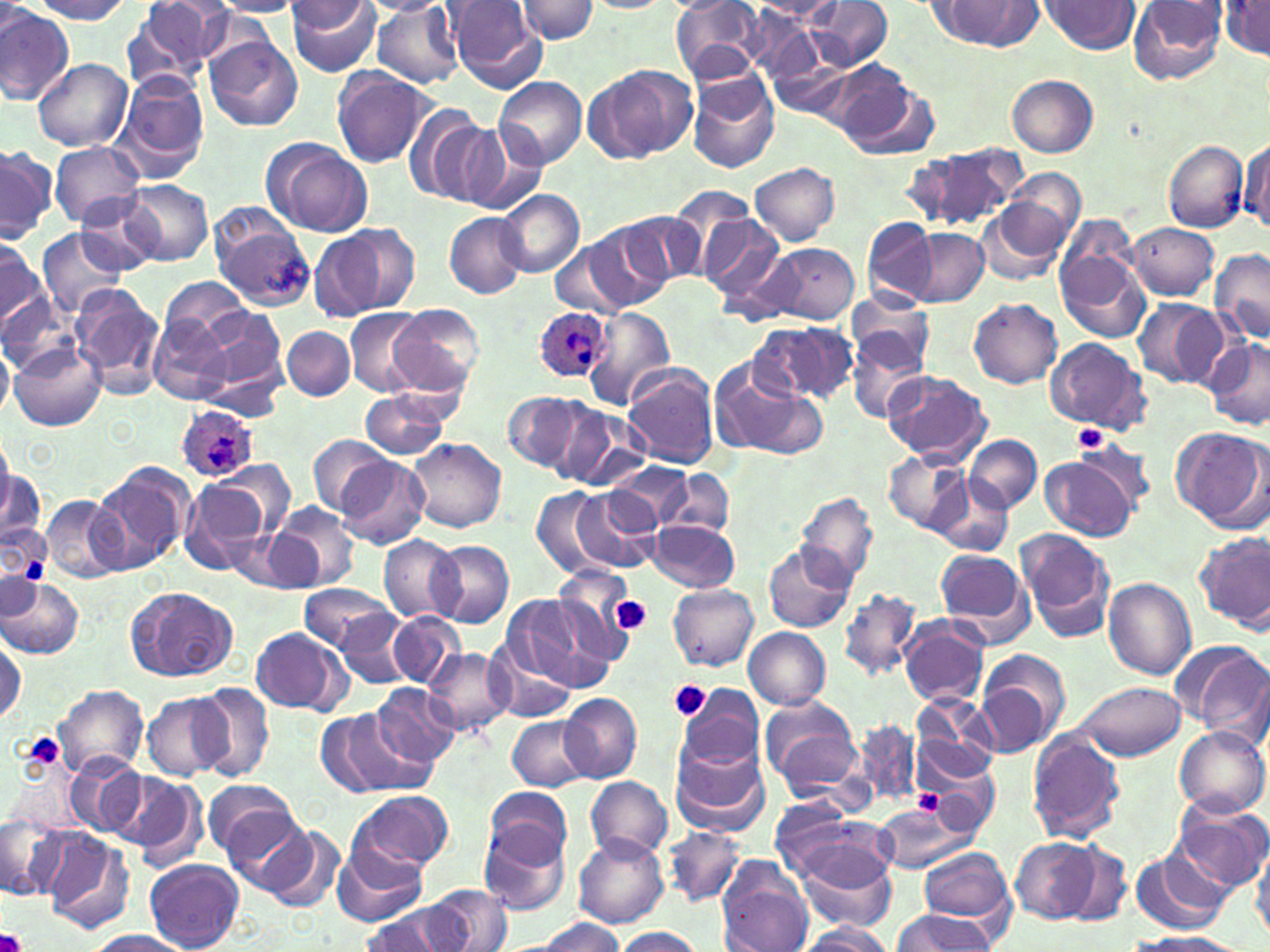
Summary:
  - Coordinate format: approximate bounding boxes as named x1/y1/x2/y2 corners in pixels
  - Plasmodium ovale-infected red blood cell locations: (x1=534, y1=305, x2=612, y2=383), (x1=174, y1=404, x2=258, y2=484)
  - Uninfected red blood cell locations: (x1=27, y1=0, x2=136, y2=23), (x1=285, y1=0, x2=382, y2=75), (x1=360, y1=0, x2=450, y2=16), (x1=753, y1=0, x2=844, y2=27), (x1=807, y1=0, x2=893, y2=71), (x1=1128, y1=0, x2=1229, y2=86), (x1=122, y1=1, x2=227, y2=92), (x1=210, y1=1, x2=302, y2=17), (x1=446, y1=1, x2=546, y2=91), (x1=514, y1=1, x2=600, y2=43), (x1=672, y1=1, x2=768, y2=81), (x1=1040, y1=1, x2=1140, y2=54), (x1=285, y1=2, x2=371, y2=33), (x1=1220, y1=2, x2=1270, y2=58), (x1=939, y1=3, x2=1044, y2=48), (x1=369, y1=4, x2=465, y2=88), (x1=0, y1=10, x2=75, y2=104), (x1=205, y1=36, x2=303, y2=131), (x1=767, y1=41, x2=860, y2=121), (x1=32, y1=58, x2=132, y2=151), (x1=587, y1=64, x2=696, y2=164), (x1=330, y1=68, x2=436, y2=168), (x1=685, y1=69, x2=781, y2=174), (x1=112, y1=70, x2=210, y2=179), (x1=834, y1=70, x2=937, y2=160), (x1=1007, y1=74, x2=1099, y2=158), (x1=495, y1=75, x2=588, y2=168), (x1=406, y1=106, x2=505, y2=207), (x1=445, y1=120, x2=544, y2=214), (x1=1239, y1=136, x2=1270, y2=234), (x1=263, y1=139, x2=373, y2=237), (x1=1162, y1=140, x2=1249, y2=233), (x1=48, y1=142, x2=147, y2=229), (x1=0, y1=145, x2=55, y2=242), (x1=916, y1=145, x2=1025, y2=235), (x1=751, y1=162, x2=840, y2=245), (x1=997, y1=171, x2=1086, y2=265), (x1=122, y1=181, x2=213, y2=265), (x1=497, y1=188, x2=585, y2=277), (x1=77, y1=196, x2=160, y2=275), (x1=979, y1=202, x2=1072, y2=287), (x1=212, y1=209, x2=317, y2=308), (x1=444, y1=211, x2=526, y2=298), (x1=623, y1=212, x2=704, y2=290), (x1=697, y1=214, x2=786, y2=301), (x1=1058, y1=215, x2=1138, y2=288), (x1=862, y1=216, x2=940, y2=304), (x1=582, y1=223, x2=670, y2=310), (x1=1126, y1=223, x2=1219, y2=299), (x1=36, y1=228, x2=130, y2=319), (x1=905, y1=228, x2=989, y2=308), (x1=308, y1=229, x2=390, y2=320), (x1=0, y1=232, x2=45, y2=327), (x1=549, y1=242, x2=630, y2=314), (x1=758, y1=244, x2=861, y2=325), (x1=1057, y1=248, x2=1151, y2=343), (x1=1211, y1=248, x2=1270, y2=346), (x1=160, y1=278, x2=253, y2=346), (x1=71, y1=283, x2=165, y2=395), (x1=0, y1=293, x2=77, y2=377), (x1=846, y1=293, x2=934, y2=376), (x1=1131, y1=297, x2=1228, y2=391), (x1=968, y1=298, x2=1062, y2=388), (x1=387, y1=305, x2=482, y2=398), (x1=357, y1=306, x2=463, y2=446), (x1=584, y1=306, x2=677, y2=411), (x1=199, y1=307, x2=288, y2=397), (x1=345, y1=309, x2=424, y2=396), (x1=148, y1=314, x2=233, y2=406), (x1=751, y1=320, x2=856, y2=406), (x1=844, y1=323, x2=931, y2=422), (x1=282, y1=326, x2=355, y2=400), (x1=1044, y1=337, x2=1150, y2=436), (x1=1204, y1=338, x2=1270, y2=433), (x1=0, y1=343, x2=14, y2=418), (x1=11, y1=343, x2=105, y2=431), (x1=707, y1=362, x2=822, y2=459), (x1=621, y1=364, x2=720, y2=467), (x1=884, y1=371, x2=991, y2=464), (x1=361, y1=392, x2=449, y2=458), (x1=504, y1=392, x2=584, y2=474), (x1=551, y1=402, x2=648, y2=491), (x1=1171, y1=428, x2=1267, y2=530), (x1=965, y1=435, x2=1041, y2=513), (x1=309, y1=436, x2=395, y2=516), (x1=1074, y1=437, x2=1159, y2=513), (x1=406, y1=438, x2=507, y2=531), (x1=883, y1=449, x2=973, y2=536), (x1=1041, y1=455, x2=1138, y2=541), (x1=334, y1=456, x2=430, y2=549), (x1=610, y1=462, x2=694, y2=534), (x1=92, y1=463, x2=194, y2=572), (x1=199, y1=465, x2=295, y2=552), (x1=0, y1=469, x2=46, y2=546), (x1=662, y1=469, x2=734, y2=539), (x1=933, y1=477, x2=1012, y2=558), (x1=180, y1=480, x2=271, y2=575), (x1=532, y1=487, x2=613, y2=577), (x1=569, y1=487, x2=658, y2=573), (x1=795, y1=492, x2=879, y2=589), (x1=40, y1=496, x2=130, y2=584), (x1=269, y1=503, x2=359, y2=593), (x1=0, y1=516, x2=51, y2=596), (x1=650, y1=519, x2=739, y2=592), (x1=1017, y1=529, x2=1115, y2=643), (x1=1197, y1=532, x2=1270, y2=634), (x1=379, y1=535, x2=462, y2=621), (x1=428, y1=539, x2=514, y2=628), (x1=764, y1=543, x2=856, y2=634), (x1=933, y1=547, x2=1033, y2=641), (x1=2, y1=570, x2=37, y2=621), (x1=551, y1=573, x2=633, y2=667), (x1=1103, y1=577, x2=1195, y2=679), (x1=0, y1=578, x2=83, y2=657), (x1=300, y1=583, x2=397, y2=652), (x1=667, y1=583, x2=758, y2=670), (x1=128, y1=587, x2=239, y2=682), (x1=838, y1=589, x2=923, y2=681), (x1=499, y1=594, x2=607, y2=693), (x1=336, y1=609, x2=416, y2=687), (x1=388, y1=611, x2=466, y2=688), (x1=899, y1=616, x2=991, y2=708), (x1=250, y1=627, x2=348, y2=715), (x1=744, y1=627, x2=831, y2=709), (x1=0, y1=633, x2=26, y2=726), (x1=488, y1=639, x2=576, y2=722), (x1=1170, y1=639, x2=1270, y2=739), (x1=423, y1=647, x2=513, y2=737), (x1=976, y1=654, x2=1066, y2=759), (x1=192, y1=681, x2=275, y2=781), (x1=1068, y1=681, x2=1188, y2=762), (x1=369, y1=682, x2=460, y2=768), (x1=55, y1=685, x2=150, y2=778), (x1=678, y1=686, x2=765, y2=776), (x1=559, y1=691, x2=642, y2=782), (x1=141, y1=693, x2=231, y2=781), (x1=759, y1=695, x2=864, y2=798), (x1=997, y1=699, x2=1100, y2=836), (x1=910, y1=701, x2=1005, y2=790), (x1=312, y1=708, x2=408, y2=796), (x1=507, y1=716, x2=591, y2=791), (x1=852, y1=718, x2=920, y2=807), (x1=1172, y1=726, x2=1269, y2=818), (x1=1026, y1=730, x2=1125, y2=844), (x1=671, y1=740, x2=769, y2=835), (x1=65, y1=756, x2=146, y2=839), (x1=922, y1=760, x2=1001, y2=834), (x1=108, y1=769, x2=203, y2=863), (x1=586, y1=776, x2=672, y2=860), (x1=202, y1=780, x2=301, y2=866), (x1=485, y1=787, x2=572, y2=870), (x1=347, y1=790, x2=453, y2=877), (x1=1169, y1=797, x2=1270, y2=892), (x1=216, y1=803, x2=317, y2=895), (x1=872, y1=803, x2=978, y2=874), (x1=776, y1=807, x2=896, y2=892), (x1=2, y1=816, x2=75, y2=904), (x1=477, y1=816, x2=573, y2=918), (x1=246, y1=821, x2=345, y2=912), (x1=662, y1=825, x2=749, y2=907), (x1=38, y1=828, x2=137, y2=935), (x1=573, y1=832, x2=670, y2=929), (x1=788, y1=832, x2=899, y2=930), (x1=1011, y1=838, x2=1098, y2=923), (x1=1061, y1=842, x2=1132, y2=926), (x1=334, y1=845, x2=426, y2=924), (x1=1249, y1=846, x2=1270, y2=943), (x1=917, y1=848, x2=1015, y2=925), (x1=1130, y1=848, x2=1231, y2=935), (x1=715, y1=858, x2=815, y2=952), (x1=144, y1=859, x2=245, y2=952), (x1=425, y1=885, x2=513, y2=951), (x1=361, y1=904, x2=463, y2=952), (x1=892, y1=910, x2=998, y2=951), (x1=528, y1=918, x2=627, y2=951), (x1=795, y1=923, x2=894, y2=952), (x1=612, y1=927, x2=704, y2=952), (x1=84, y1=929, x2=192, y2=952), (x1=1131, y1=932, x2=1244, y2=952)
  - Platelet locations: (x1=1074, y1=423, x2=1110, y2=452), (x1=609, y1=596, x2=651, y2=634), (x1=668, y1=681, x2=710, y2=723), (x1=16, y1=732, x2=64, y2=776), (x1=914, y1=788, x2=946, y2=816), (x1=0, y1=928, x2=27, y2=952)
  - Slide-level diagnosis: Plasmodium ovale
  - Magnification: 1000x
  - Image size: 1270×952 pixels
  - Preparation: thin blood film
  - Stain: May-Grünwald-Giemsa
  - Field of view: one of a larger specimen
  - Modality: optical microscopy